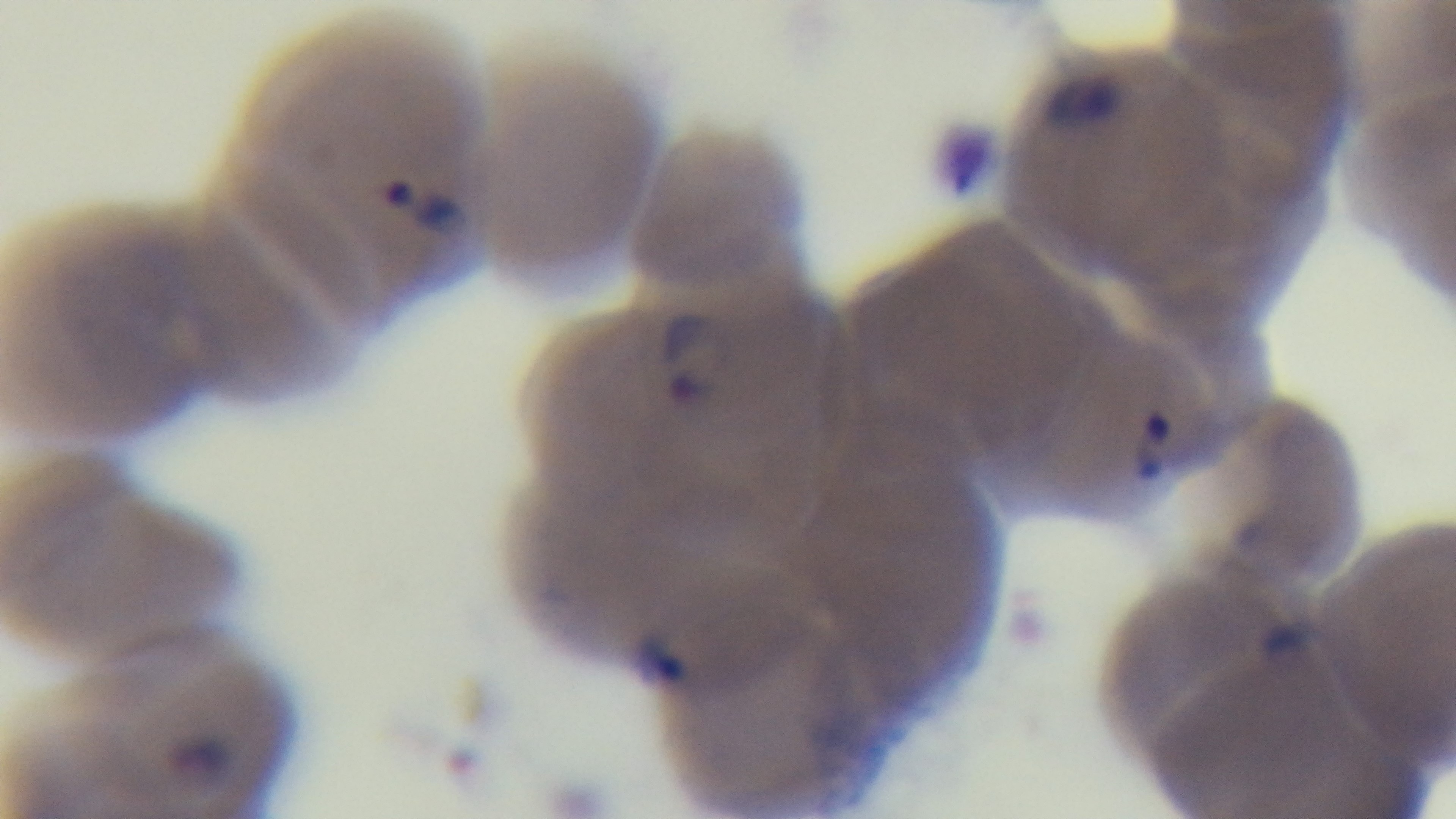
modality: light microscopy
objective: 100x oil immersion
malaria_status: infected
stain: Giemsa
capture: mounted 4K digital camera
preparation: thin smear
field_of_view: one from the slide